Outline each blood parasite and name the species.
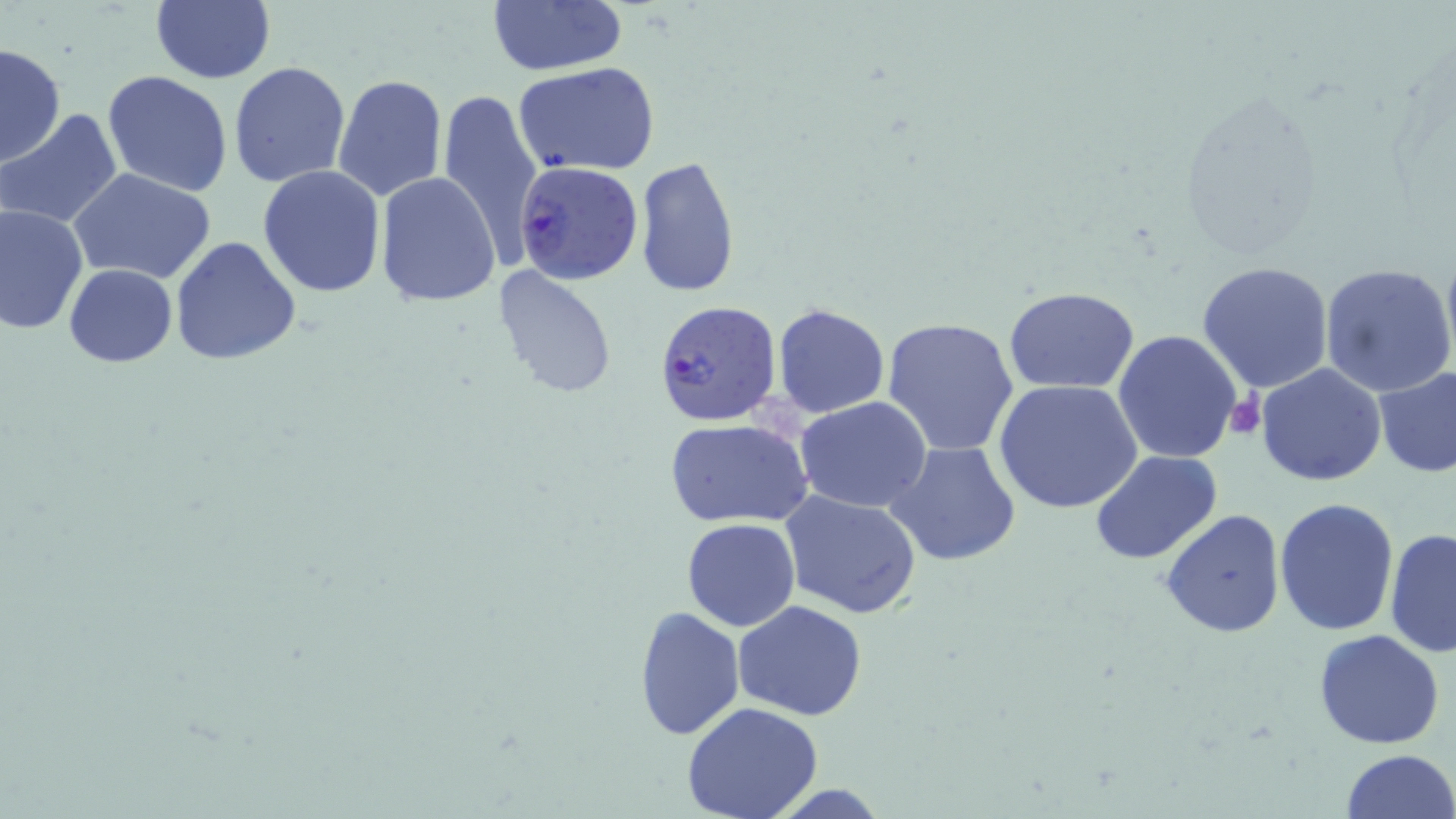
Approximate bounding boxes as named x1/y1/x2/y2 corners in pixels.
Plasmodium falciparum-infected red blood cells: (x1=513, y1=160, x2=643, y2=284), (x1=654, y1=301, x2=782, y2=427).
No Plasmodium ovale, Plasmodium malariae, Plasmodium vivax, Babesia divergens, or Trypanosoma brucei observed.

{
  "slide_level_diagnosis": "Plasmodium falciparum",
  "stain": "May-Grünwald-Giemsa",
  "image_size": "1456×819 pixels",
  "field_of_view": "one of a larger specimen",
  "magnification": "1000x",
  "preparation": "thin blood film",
  "modality": "light microscopy",
  "platelet_locations": "approximate bounding boxes as named x1/y1/x2/y2 corners in pixels: (x1=1223, y1=394, x2=1267, y2=439)",
  "uninfected_red_blood_cell_locations": "approximate bounding boxes as named x1/y1/x2/y2 corners in pixels: (x1=149, y1=0, x2=275, y2=84), (x1=486, y1=2, x2=625, y2=76), (x1=1, y1=44, x2=66, y2=167), (x1=514, y1=60, x2=661, y2=176), (x1=227, y1=62, x2=352, y2=189), (x1=102, y1=70, x2=234, y2=197), (x1=334, y1=74, x2=449, y2=203), (x1=1171, y1=85, x2=1328, y2=261), (x1=435, y1=86, x2=545, y2=266), (x1=0, y1=110, x2=124, y2=228), (x1=634, y1=156, x2=740, y2=298), (x1=258, y1=165, x2=386, y2=299), (x1=68, y1=166, x2=218, y2=284), (x1=374, y1=173, x2=501, y2=306), (x1=0, y1=202, x2=87, y2=334), (x1=169, y1=237, x2=301, y2=365), (x1=1196, y1=261, x2=1334, y2=394), (x1=1318, y1=263, x2=1456, y2=399), (x1=64, y1=264, x2=177, y2=367), (x1=492, y1=267, x2=618, y2=398), (x1=1005, y1=286, x2=1139, y2=394), (x1=772, y1=303, x2=891, y2=419), (x1=882, y1=317, x2=1020, y2=456), (x1=1112, y1=329, x2=1244, y2=465), (x1=1256, y1=363, x2=1387, y2=485), (x1=1372, y1=365, x2=1456, y2=478), (x1=994, y1=379, x2=1143, y2=515), (x1=794, y1=397, x2=934, y2=513), (x1=667, y1=419, x2=812, y2=529), (x1=888, y1=442, x2=1021, y2=568), (x1=1089, y1=450, x2=1223, y2=565), (x1=780, y1=489, x2=921, y2=618), (x1=1273, y1=498, x2=1397, y2=635), (x1=1160, y1=508, x2=1286, y2=640), (x1=681, y1=518, x2=800, y2=631), (x1=1385, y1=527, x2=1455, y2=658), (x1=733, y1=600, x2=868, y2=720), (x1=632, y1=605, x2=743, y2=742), (x1=1312, y1=629, x2=1446, y2=749), (x1=681, y1=702, x2=824, y2=819), (x1=1339, y1=749, x2=1454, y2=819)"
}